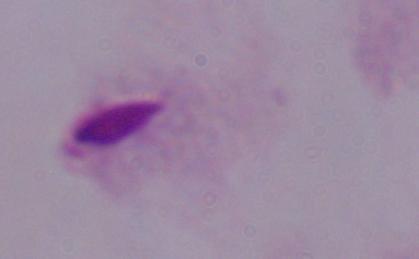

A trichomonad is shown. Captured at 1000x magnification. Micrograph.